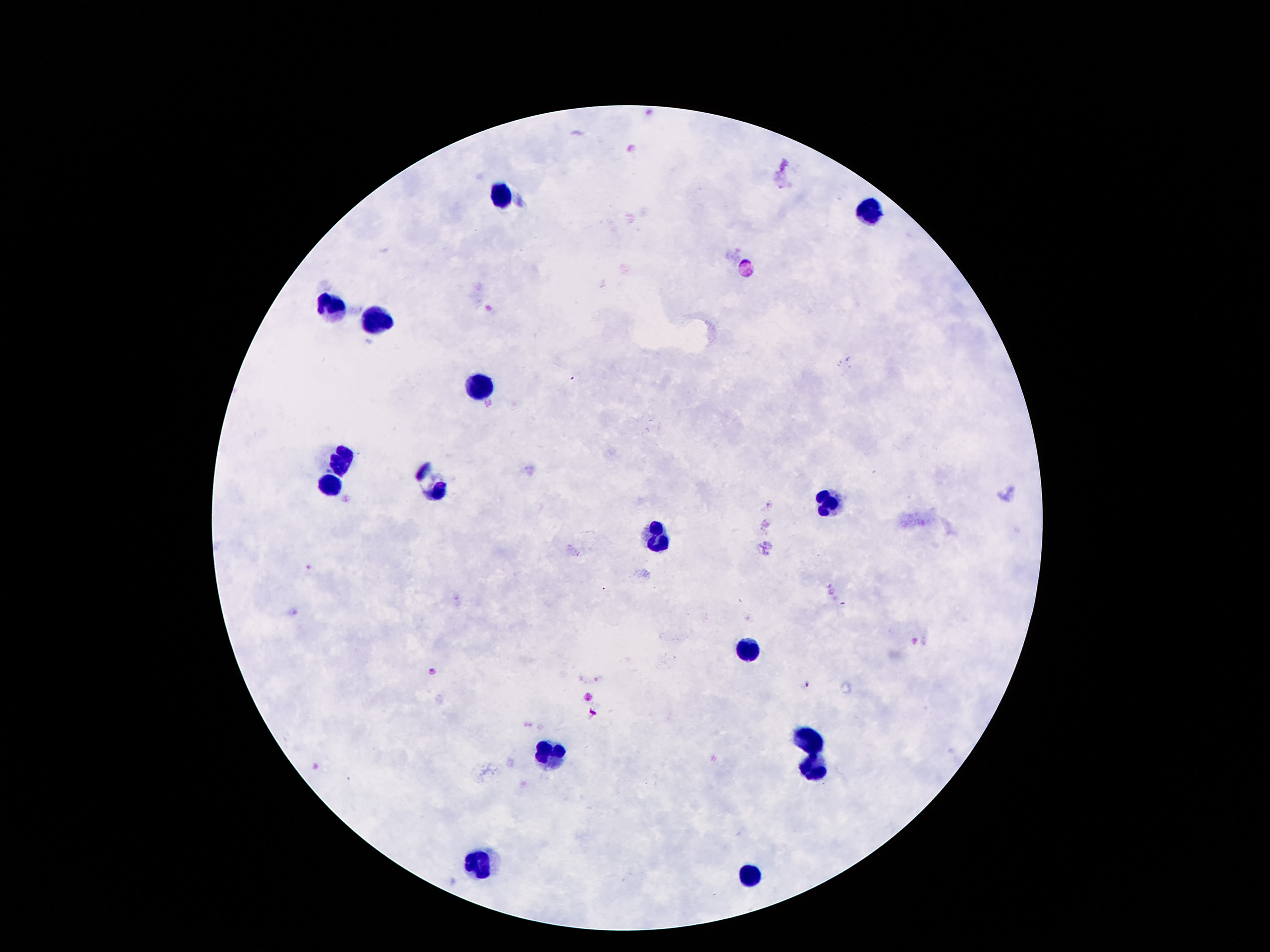 Approximate centers as {x, y} in pixels. Leukocyte locations: {498, 194}, {869, 212}, {330, 304}, {381, 319}, {477, 386}, {340, 463}, {330, 484}, {430, 490}, {828, 501}, {662, 537}, {744, 652}, {809, 738}, {549, 755}, {809, 771}, {479, 863}, {750, 878}. Image is 1270×952 pixels. Patient malaria status: uninfected. 100x magnification. Photographed through the microscope eyepiece with a smartphone camera. One field from this slide. Thick peripheral-blood smear. Giemsa-stained preparation.